Locate every blood parasite and identify its species.
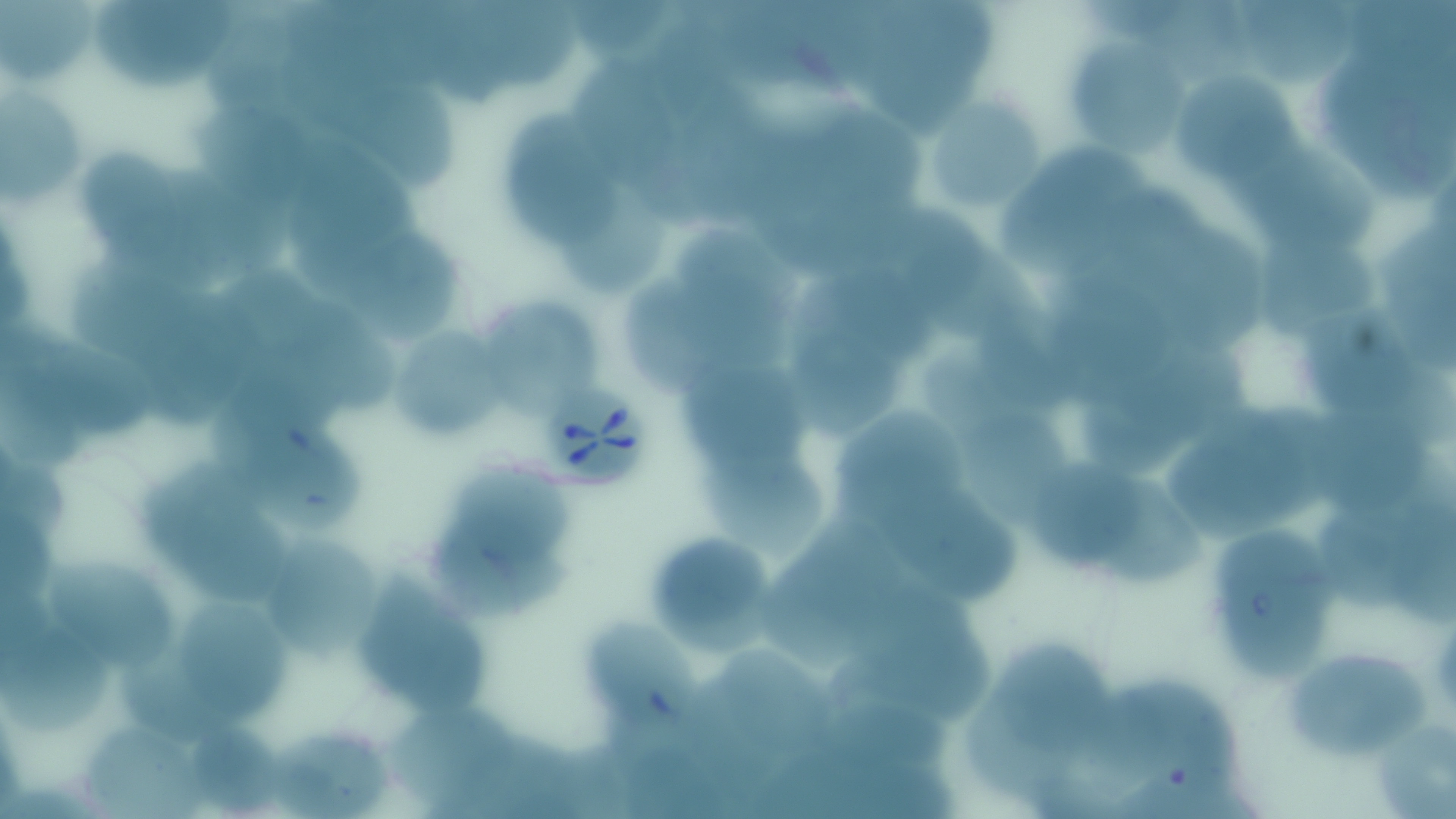
Approximate bounding boxes as [x1, y1, x2, y2] in pixels.
Babesia divergens-infected red blood cells: [540, 379, 656, 492].
No Plasmodium falciparum, Plasmodium ovale, Plasmodium malariae, Plasmodium vivax, or Trypanosoma brucei observed.

{
  "slide_level_diagnosis": "Babesia divergens",
  "magnification": "1000x",
  "field_of_view": "one of a larger specimen",
  "image_size": "1456×819 pixels",
  "uninfected_red_blood_cell_locations": "approximate bounding boxes as [x1, y1, x2, y2] in pixels: [1, 0, 102, 91], [569, 0, 682, 57], [1237, 0, 1354, 89], [94, 1, 240, 85], [468, 2, 584, 93], [1071, 33, 1188, 163], [281, 37, 401, 141], [576, 53, 673, 183], [1174, 67, 1307, 183], [307, 76, 463, 192], [0, 88, 83, 214], [934, 97, 1044, 209], [178, 98, 320, 212], [813, 108, 932, 209], [507, 122, 627, 253], [286, 135, 420, 291], [1003, 144, 1151, 277], [1232, 144, 1385, 251], [74, 146, 185, 264], [1107, 183, 1221, 293], [560, 185, 671, 294], [889, 205, 994, 317], [338, 211, 456, 351], [1148, 221, 1286, 359], [681, 227, 799, 330], [1261, 228, 1381, 346], [912, 241, 1047, 344], [828, 264, 942, 364], [620, 266, 721, 398], [69, 271, 197, 363], [1050, 280, 1178, 399], [162, 282, 277, 419], [292, 297, 405, 415], [485, 298, 604, 415], [1306, 304, 1419, 415], [976, 306, 1079, 408], [777, 310, 904, 441], [392, 318, 505, 432], [13, 326, 162, 439], [1122, 338, 1267, 436], [683, 347, 804, 475], [2, 377, 88, 473], [1079, 395, 1194, 473], [1314, 398, 1428, 512], [829, 400, 971, 525], [238, 406, 366, 532], [1166, 406, 1330, 548], [965, 419, 1068, 512], [699, 438, 829, 566], [1028, 446, 1150, 577], [452, 453, 577, 578], [0, 457, 74, 536], [144, 470, 292, 603], [1101, 474, 1202, 591], [884, 489, 1022, 606], [1315, 493, 1436, 609], [1392, 500, 1456, 628], [0, 505, 56, 606], [796, 512, 906, 627], [1216, 517, 1330, 685], [420, 530, 577, 621], [640, 530, 778, 651], [260, 533, 377, 660], [357, 559, 494, 718], [761, 559, 868, 672], [49, 562, 179, 676], [174, 595, 293, 727], [834, 599, 993, 730], [587, 616, 705, 740], [5, 621, 113, 736], [119, 636, 224, 747], [994, 641, 1114, 756], [1287, 645, 1429, 760], [720, 649, 835, 752], [1097, 675, 1242, 794], [809, 687, 961, 783], [963, 691, 1083, 801], [391, 703, 520, 809], [191, 718, 285, 813], [1379, 720, 1456, 819], [83, 726, 205, 819], [276, 728, 394, 817], [460, 729, 585, 819], [620, 738, 736, 819]",
  "modality": "optical microscopy",
  "stain": "May-Grünwald-Giemsa",
  "preparation": "thin blood film"
}